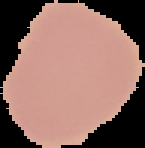

Summary:
  - Image size: 145×148 pixels
  - Image type: cell region segmented out of the field of view; surrounding area masked to black
  - Preparation: thin blood film
  - Result: negative for Plasmodium parasites